Classify this cell by malaria status.
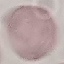

Uninfected.

Giemsa-stained preparation. Photographed with a smartphone camera at the microscope eyepiece. Thin blood smear. Cell patch, automatically extracted from a larger field of view and resized to 64 × 64 pixels.